Report the malaria status of this cell.
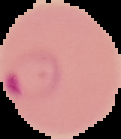

It is parasitized.

Image is 121×139 pixels. Segmented cell region on a black background. From a thin blood film.